Point out Plasmodium parasites and leukocytes.
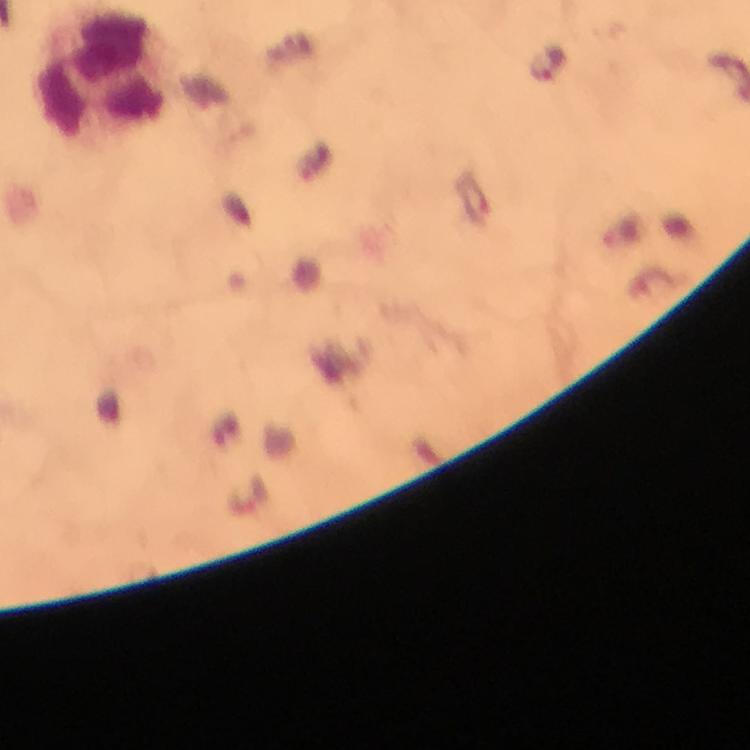
Approximate centers as {x, y} in pixels.
Plasmodium parasites: {546, 62}.
Leukocytes: {103, 78}.

Image is 750×750 pixels. Cropped region of a single field of view. Thick blood film. Giemsa-stained preparation. Immersion oil applied. From a malaria diagnostic workup. At 100x magnification. Smartphone photograph taken through a microscope.